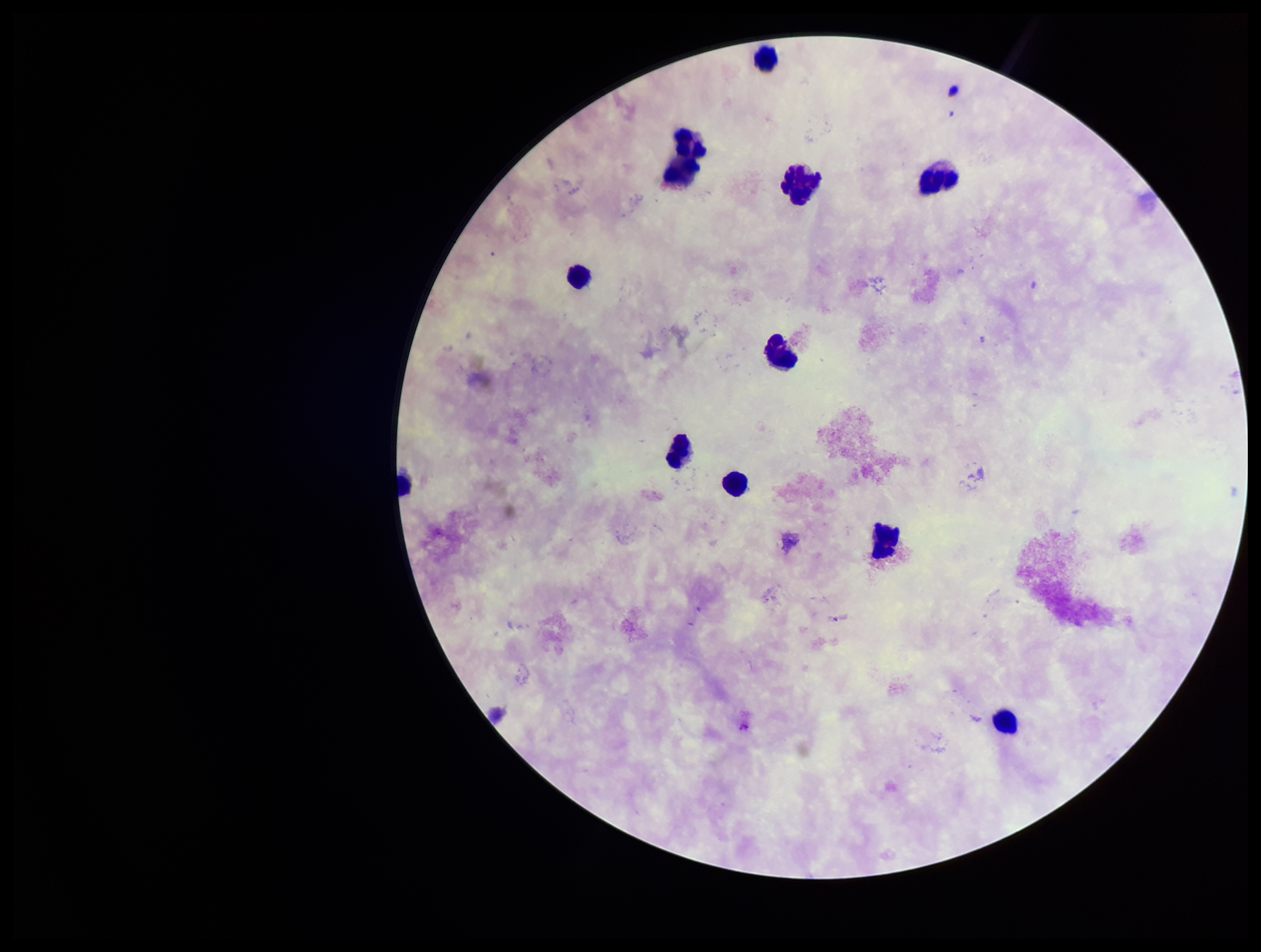
Summary:
  - Image size: 1261×952 pixels
  - Field of view: one from this slide
  - Leukocyte count: 11
  - Capture: smartphone photograph through the microscope eyepiece
  - Parasite count: 0
  - Patient malaria status: negative
  - Stain: Giemsa
  - Plasmodium parasites: none seen
  - Preparation: thick